Comment on the morphology of the red blood cells.
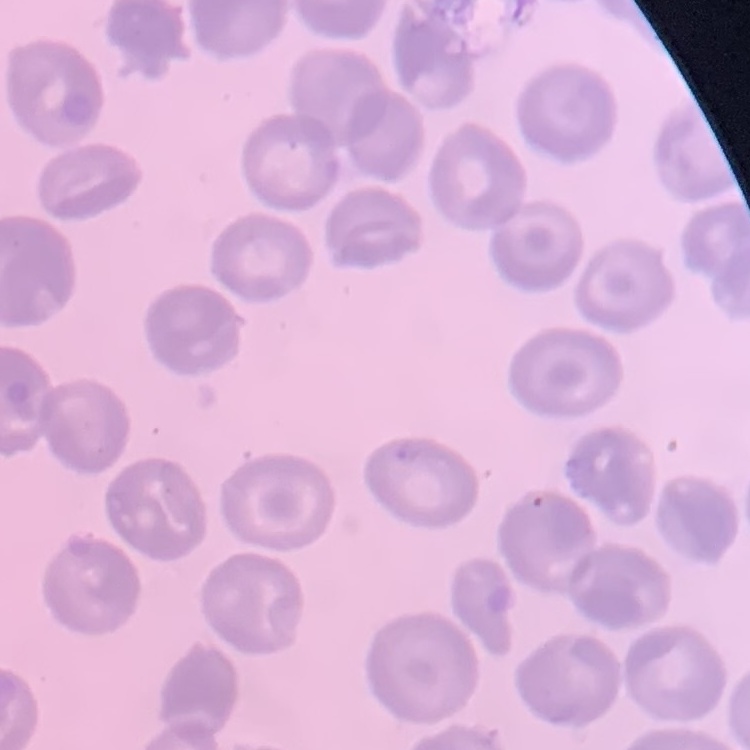
No rouleaux formation.

preparation = thin blood film
image type = square crop of a larger photomicrograph
stain = Field's or Giemsa